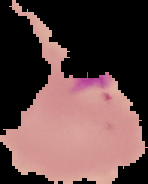
The area outside the segmented cell region is set to black. From a thin blood film. Image is 148×184 pixels. Malaria status: parasitized.